Report the malaria status of this cell.
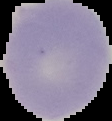
Uninfected.

image type = segmented cell region on a black background
image size = 112×121 pixels
preparation = thin blood smear